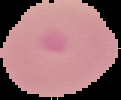
From a thin blood film. Cell region segmented out of the field of view; the surrounding area is masked to black. Image is 121×100 pixels. Malaria status: parasitized.